Classify this cell by malaria status.
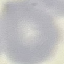
Uninfected.

Cell patch, automatically extracted from a larger field of view and resized to 64 × 64 pixels. Acquired by smartphone through the microscope eyepiece. Giemsa stain. Thin blood film.